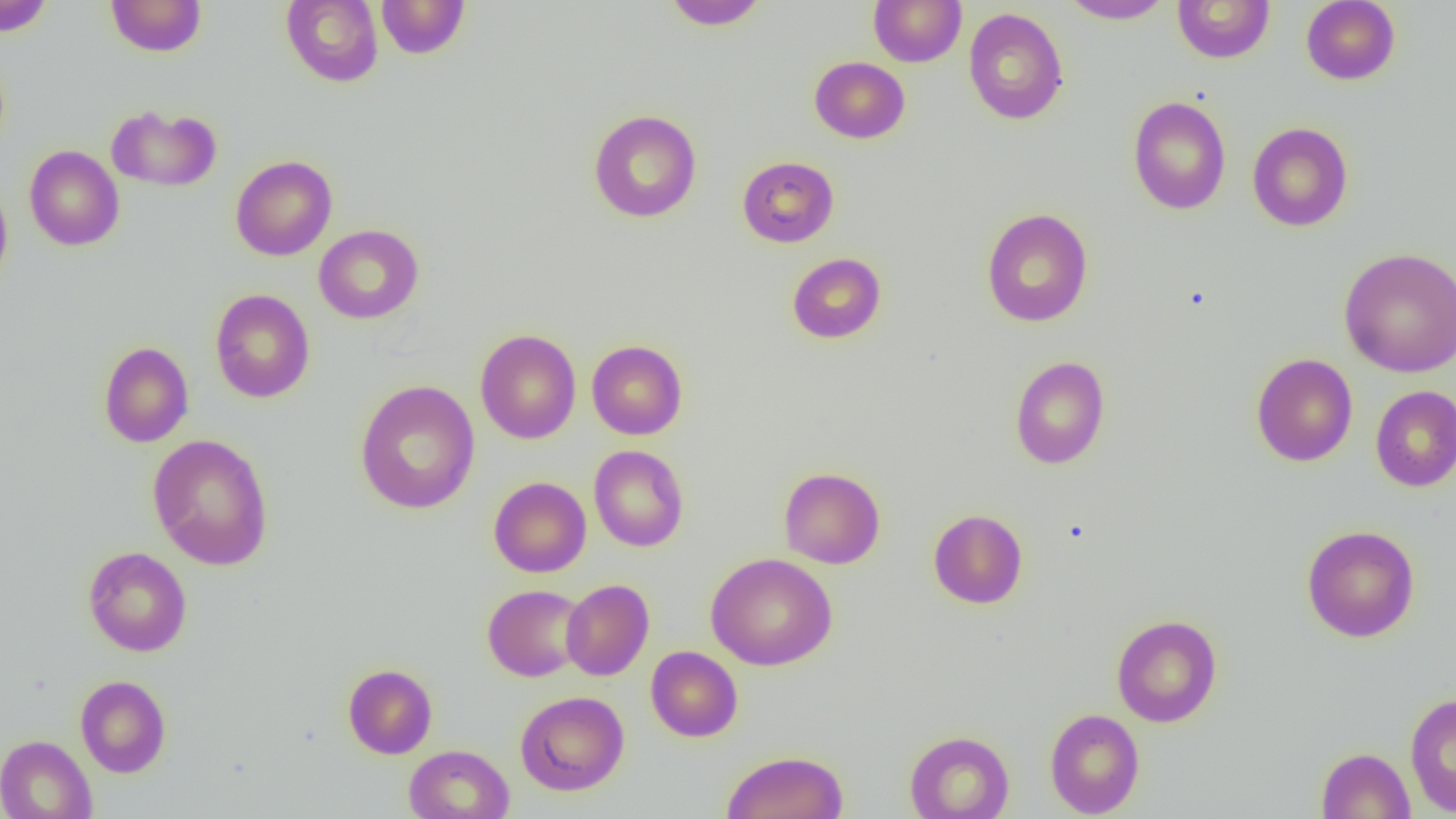
Summary:
  - Coordinate format: approximate bounding boxes as named x1/y1/x2/y2 corners in pixels
  - Uninfected red blood cell locations: (x1=0, y1=0, x2=56, y2=37), (x1=105, y1=0, x2=208, y2=57), (x1=281, y1=0, x2=383, y2=87), (x1=376, y1=0, x2=471, y2=58), (x1=661, y1=0, x2=770, y2=30), (x1=868, y1=0, x2=967, y2=67), (x1=1058, y1=0, x2=1175, y2=24), (x1=1301, y1=0, x2=1401, y2=85), (x1=1172, y1=1, x2=1275, y2=63), (x1=963, y1=8, x2=1068, y2=125), (x1=809, y1=56, x2=910, y2=143), (x1=1128, y1=96, x2=1231, y2=215), (x1=107, y1=104, x2=221, y2=192), (x1=588, y1=109, x2=702, y2=223), (x1=1247, y1=122, x2=1353, y2=231), (x1=24, y1=145, x2=125, y2=251), (x1=230, y1=155, x2=337, y2=261), (x1=737, y1=156, x2=839, y2=247), (x1=0, y1=180, x2=13, y2=292), (x1=980, y1=207, x2=1093, y2=327), (x1=314, y1=224, x2=424, y2=324), (x1=1339, y1=247, x2=1456, y2=378), (x1=786, y1=252, x2=886, y2=344), (x1=210, y1=289, x2=315, y2=403), (x1=475, y1=329, x2=581, y2=444), (x1=586, y1=340, x2=687, y2=440), (x1=98, y1=341, x2=193, y2=447), (x1=1251, y1=353, x2=1358, y2=466), (x1=1009, y1=355, x2=1110, y2=469), (x1=355, y1=380, x2=480, y2=514), (x1=1370, y1=385, x2=1456, y2=492), (x1=148, y1=433, x2=274, y2=571), (x1=589, y1=445, x2=688, y2=551), (x1=779, y1=467, x2=885, y2=569), (x1=489, y1=476, x2=591, y2=577), (x1=928, y1=509, x2=1028, y2=609), (x1=1301, y1=524, x2=1420, y2=642), (x1=83, y1=546, x2=192, y2=656), (x1=705, y1=552, x2=837, y2=670), (x1=561, y1=579, x2=654, y2=680), (x1=483, y1=584, x2=587, y2=681), (x1=1111, y1=614, x2=1223, y2=727), (x1=646, y1=646, x2=743, y2=741), (x1=342, y1=664, x2=437, y2=759), (x1=75, y1=675, x2=171, y2=777), (x1=515, y1=691, x2=629, y2=795), (x1=1404, y1=692, x2=1456, y2=817), (x1=1044, y1=708, x2=1145, y2=817), (x1=904, y1=730, x2=1014, y2=819), (x1=0, y1=735, x2=97, y2=819), (x1=404, y1=744, x2=514, y2=819), (x1=1316, y1=747, x2=1416, y2=818), (x1=721, y1=750, x2=848, y2=819)
  - Slide-level diagnosis: no evidence of blood parasites
  - Magnification: 1000x
  - Image size: 1456×819 pixels
  - Preparation: thin blood smear
  - Field of view: one of a larger specimen
  - Modality: light microscopy